Identify the blood parasite species.
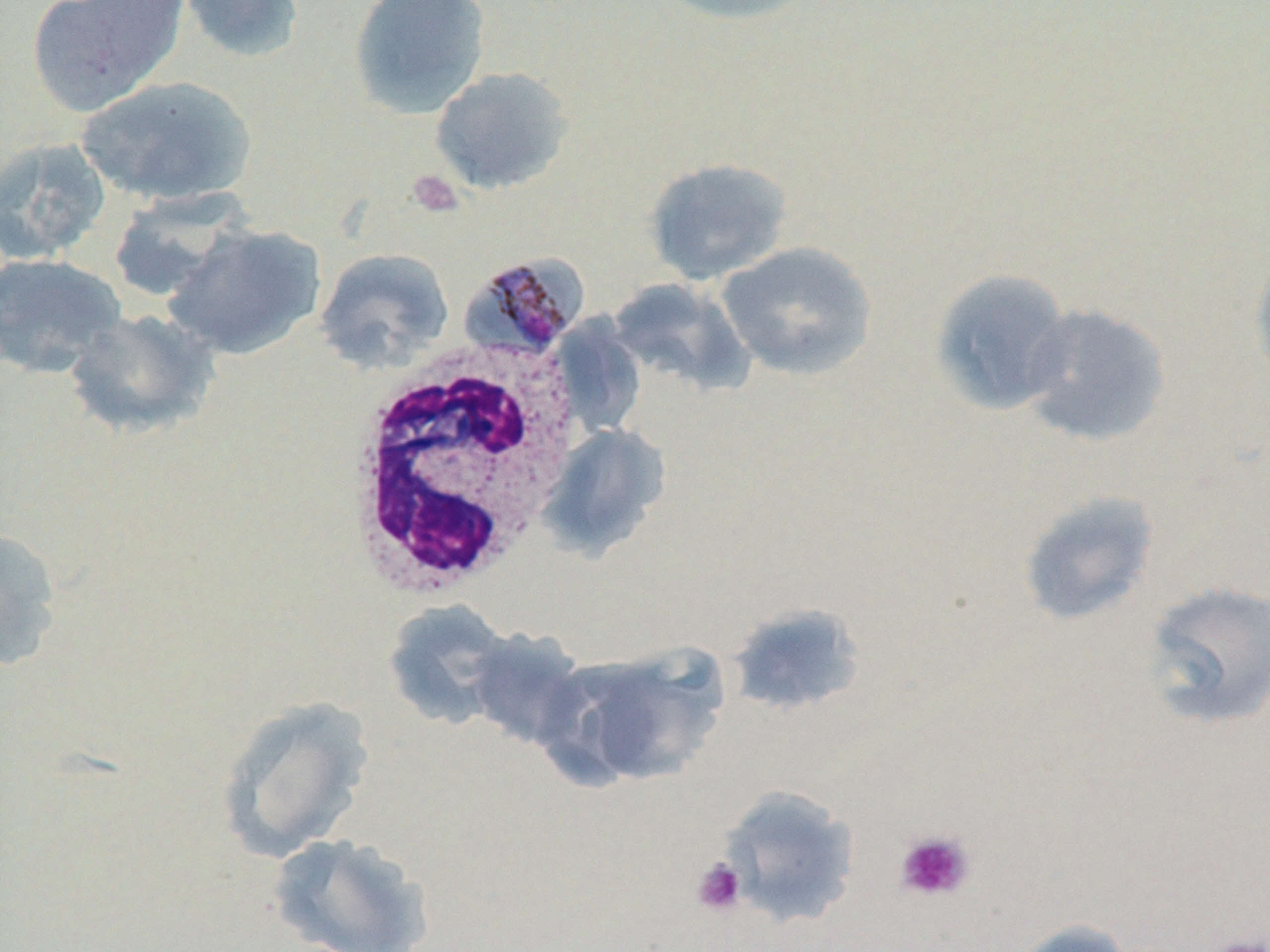
Plasmodium malariae.

image size = 1270×952 pixels
platelet locations = approximate bounding boxes as [x1, y1, x2, y2] in pixels: [407, 169, 464, 219], [894, 828, 976, 903], [691, 858, 747, 916], [1204, 932, 1267, 952]
magnification = 1000x
Plasmodium malariae-infected red blood cell locations = approximate bounding boxes as [x1, y1, x2, y2] in pixels: [460, 254, 589, 361]
white blood cell locations = approximate bounding boxes as [x1, y1, x2, y2] in pixels: [336, 339, 585, 599]
uninfected red blood cell locations = approximate bounding boxes as [x1, y1, x2, y2] in pixels: [26, 0, 188, 117], [176, 0, 306, 63], [652, 0, 818, 26], [348, 1, 491, 119], [429, 66, 574, 195], [76, 75, 255, 207], [0, 136, 112, 264], [642, 157, 793, 285], [106, 190, 249, 304], [162, 224, 326, 360], [715, 241, 877, 381], [314, 247, 455, 372], [1248, 250, 1270, 392], [0, 252, 128, 377], [929, 268, 1076, 417], [606, 278, 753, 396], [1019, 303, 1171, 448], [62, 308, 221, 440], [535, 422, 671, 561], [1017, 489, 1160, 627], [0, 525, 65, 673], [1140, 580, 1270, 731], [382, 599, 514, 729], [725, 602, 867, 716], [464, 628, 592, 750], [544, 644, 727, 790], [214, 695, 377, 863], [718, 785, 861, 929], [267, 832, 433, 952], [1006, 919, 1137, 952]
preparation = thin blood smear
modality = light microscopy
stain = May-Grünwald-Giemsa
field of view = one of a larger specimen